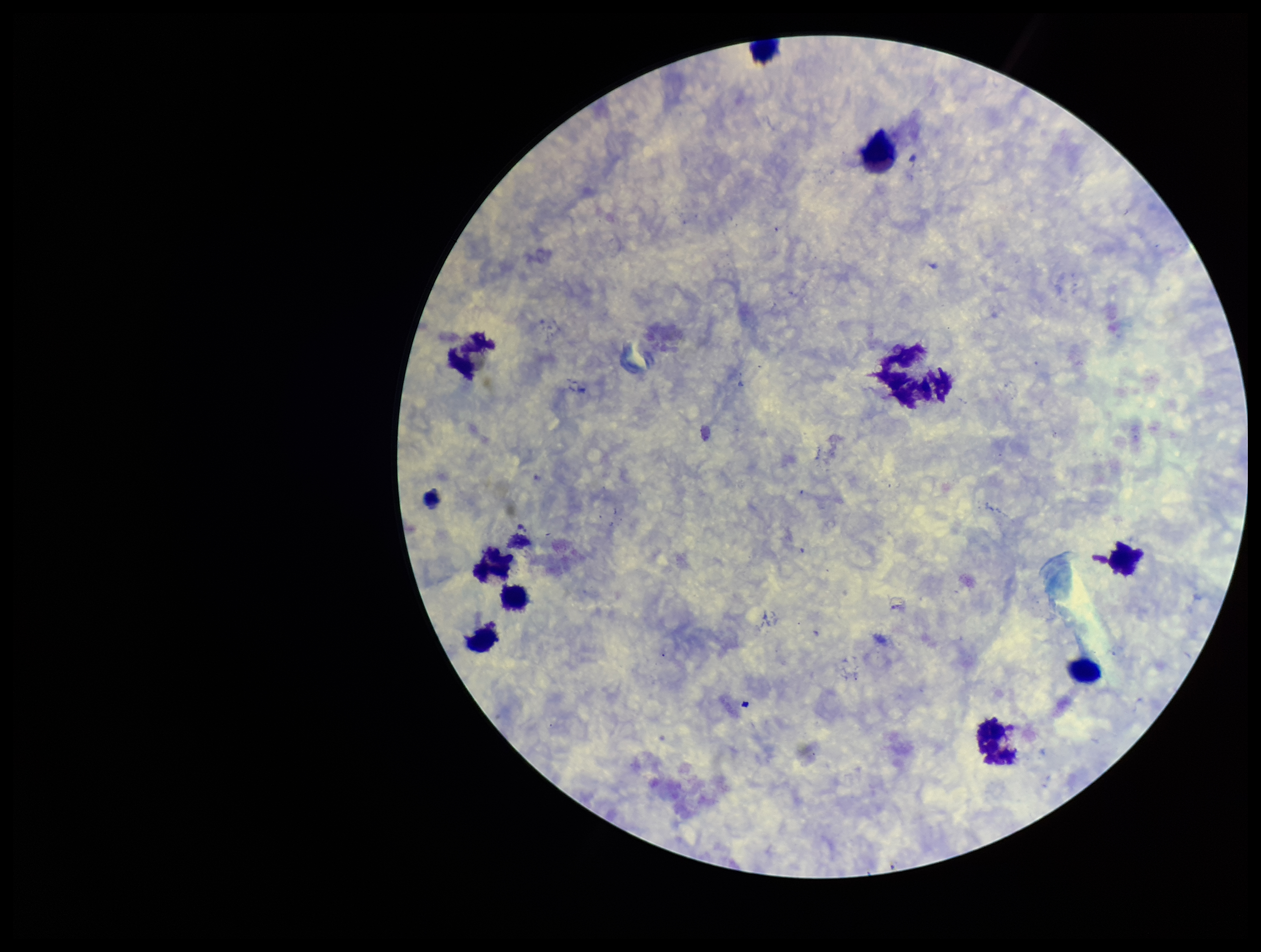

Summary:
  - Parasite count: 0
  - Plasmodium parasites: none seen
  - Image size: 1261×952 pixels
  - Leukocyte count: 10
  - Preparation: thick blood smear
  - Field of view: single
  - Patient malaria status: negative
  - Capture: smartphone photograph through the microscope eyepiece
  - Stain: Giemsa